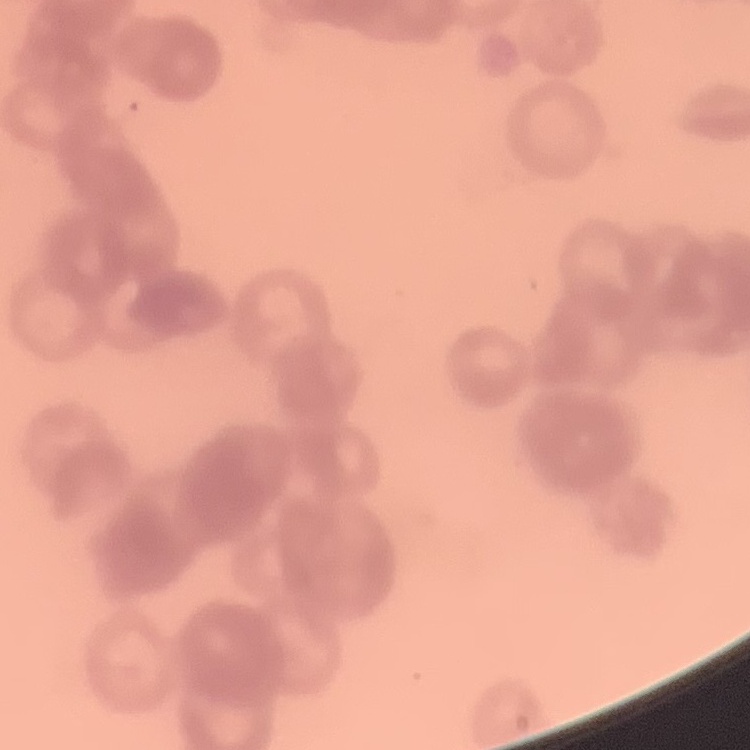

red blood cell morphology = rouleaux formation
preparation = thin peripheral smear
stain = Field's or Giemsa
image type = one tile cut from a larger photomicrograph